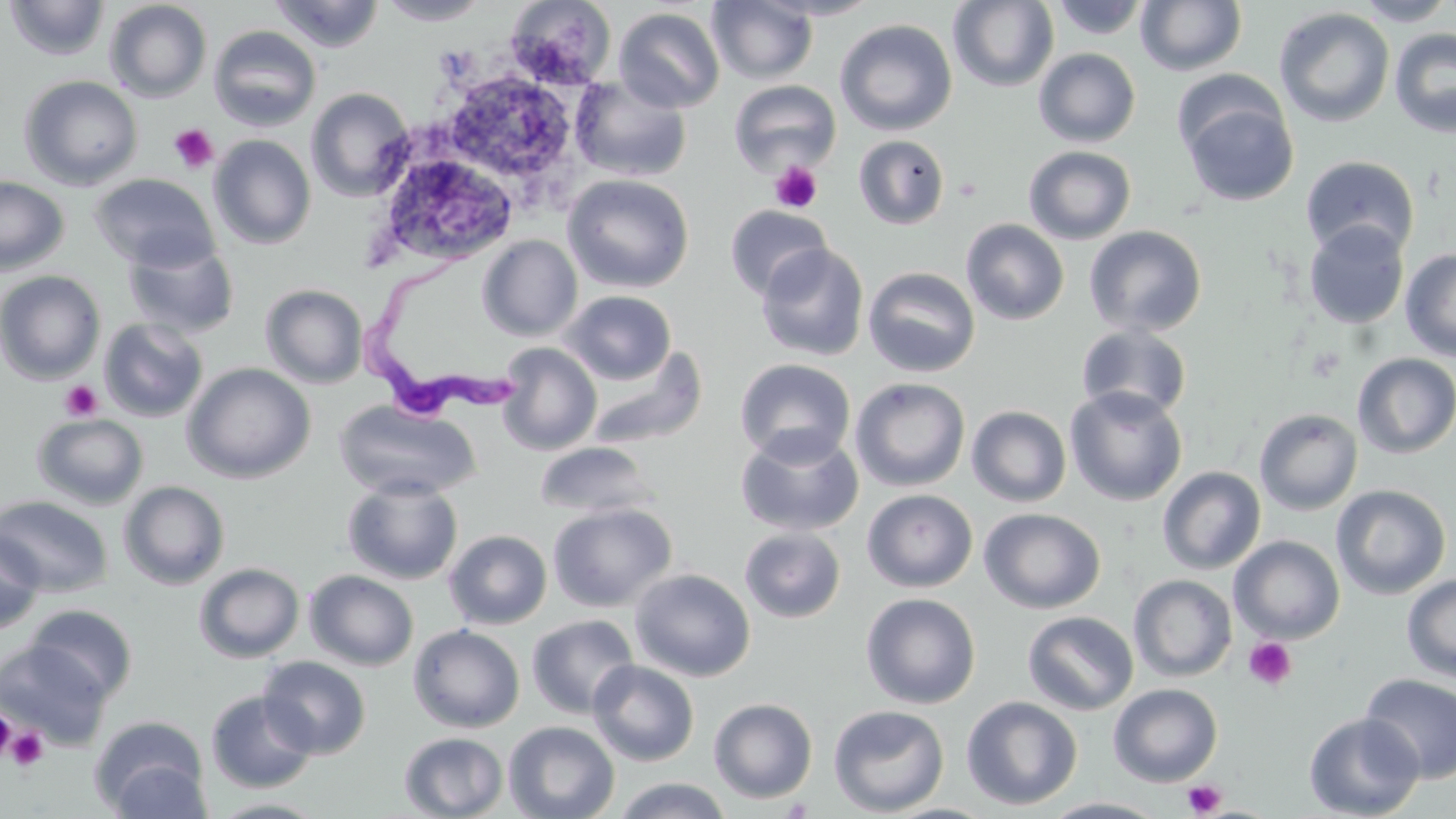
Approximate bounding boxes as named x1/y1/x2/y2 corners in pixels. Platelet locations: (x1=168, y1=123, x2=218, y2=173), (x1=770, y1=161, x2=823, y2=213), (x1=954, y1=174, x2=984, y2=200), (x1=59, y1=380, x2=103, y2=422), (x1=1243, y1=636, x2=1297, y2=691), (x1=1, y1=708, x2=16, y2=762), (x1=5, y1=726, x2=49, y2=772), (x1=1183, y1=779, x2=1227, y2=817). Uninfected red blood cell locations: (x1=3, y1=0, x2=111, y2=62), (x1=269, y1=0, x2=385, y2=52), (x1=377, y1=0, x2=490, y2=25), (x1=505, y1=0, x2=616, y2=89), (x1=758, y1=0, x2=884, y2=20), (x1=1050, y1=0, x2=1151, y2=40), (x1=1135, y1=0, x2=1247, y2=76), (x1=1351, y1=0, x2=1455, y2=26), (x1=104, y1=1, x2=212, y2=103), (x1=707, y1=1, x2=818, y2=84), (x1=948, y1=1, x2=1059, y2=92), (x1=613, y1=7, x2=725, y2=113), (x1=1274, y1=7, x2=1395, y2=128), (x1=834, y1=18, x2=957, y2=136), (x1=208, y1=24, x2=322, y2=132), (x1=1389, y1=27, x2=1456, y2=138), (x1=1033, y1=48, x2=1141, y2=147), (x1=18, y1=75, x2=143, y2=191), (x1=444, y1=76, x2=572, y2=180), (x1=568, y1=77, x2=693, y2=183), (x1=728, y1=79, x2=842, y2=179), (x1=306, y1=87, x2=414, y2=202), (x1=1179, y1=90, x2=1299, y2=207), (x1=853, y1=134, x2=950, y2=229), (x1=209, y1=135, x2=316, y2=250), (x1=1023, y1=145, x2=1137, y2=245), (x1=377, y1=149, x2=520, y2=267), (x1=1300, y1=155, x2=1420, y2=261), (x1=90, y1=172, x2=219, y2=271), (x1=562, y1=173, x2=695, y2=293), (x1=0, y1=175, x2=69, y2=275), (x1=725, y1=205, x2=832, y2=301), (x1=960, y1=219, x2=1070, y2=325), (x1=1303, y1=220, x2=1410, y2=329), (x1=1083, y1=225, x2=1207, y2=337), (x1=477, y1=235, x2=582, y2=341), (x1=123, y1=237, x2=239, y2=338), (x1=755, y1=243, x2=869, y2=362), (x1=1400, y1=248, x2=1456, y2=361), (x1=863, y1=266, x2=981, y2=378), (x1=0, y1=270, x2=106, y2=384), (x1=260, y1=284, x2=368, y2=388), (x1=559, y1=289, x2=677, y2=385), (x1=98, y1=317, x2=209, y2=422), (x1=1075, y1=323, x2=1194, y2=422), (x1=496, y1=342, x2=602, y2=454), (x1=585, y1=344, x2=708, y2=450), (x1=1352, y1=353, x2=1456, y2=458), (x1=734, y1=358, x2=856, y2=465), (x1=182, y1=362, x2=317, y2=484), (x1=850, y1=377, x2=971, y2=492), (x1=1065, y1=386, x2=1188, y2=506), (x1=333, y1=399, x2=479, y2=501), (x1=966, y1=405, x2=1072, y2=507), (x1=1254, y1=408, x2=1363, y2=515), (x1=32, y1=413, x2=149, y2=509), (x1=736, y1=427, x2=864, y2=537), (x1=534, y1=441, x2=660, y2=521), (x1=1157, y1=466, x2=1266, y2=575), (x1=342, y1=477, x2=464, y2=584), (x1=118, y1=481, x2=231, y2=590), (x1=1330, y1=484, x2=1451, y2=600), (x1=862, y1=489, x2=978, y2=593), (x1=0, y1=495, x2=113, y2=597), (x1=547, y1=501, x2=678, y2=612), (x1=978, y1=507, x2=1105, y2=614), (x1=441, y1=520, x2=681, y2=625), (x1=739, y1=527, x2=846, y2=623), (x1=0, y1=529, x2=45, y2=635), (x1=444, y1=530, x2=552, y2=630), (x1=1229, y1=535, x2=1345, y2=643), (x1=193, y1=562, x2=304, y2=663), (x1=629, y1=568, x2=756, y2=682), (x1=304, y1=570, x2=419, y2=671), (x1=1401, y1=573, x2=1456, y2=682), (x1=1128, y1=574, x2=1237, y2=682), (x1=860, y1=592, x2=981, y2=709), (x1=25, y1=604, x2=138, y2=704), (x1=1022, y1=611, x2=1139, y2=715), (x1=526, y1=614, x2=640, y2=719), (x1=408, y1=624, x2=525, y2=732), (x1=0, y1=641, x2=111, y2=749), (x1=257, y1=655, x2=372, y2=759), (x1=588, y1=660, x2=700, y2=766), (x1=1359, y1=673, x2=1456, y2=783), (x1=1108, y1=683, x2=1223, y2=786), (x1=205, y1=690, x2=318, y2=793), (x1=961, y1=696, x2=1083, y2=811), (x1=708, y1=697, x2=818, y2=803), (x1=828, y1=704, x2=950, y2=816), (x1=1303, y1=712, x2=1425, y2=818), (x1=90, y1=717, x2=211, y2=817), (x1=503, y1=721, x2=620, y2=819), (x1=399, y1=731, x2=509, y2=819), (x1=611, y1=777, x2=733, y2=819), (x1=208, y1=797, x2=328, y2=818), (x1=1039, y1=797, x2=1170, y2=818). Trypanosoma brucei locations: (x1=357, y1=240, x2=521, y2=428). Slide-level diagnosis: Trypanosoma brucei. May-Grünwald-Giemsa-stained preparation. One field of a larger specimen. Thin blood film. 1000x magnification. Light microscopy. Image is 1456×819 pixels.